Assess this cell for malaria.
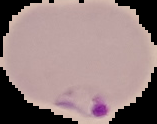
It is parasitized.

From a thin blood film. Cell region segmented out of the field of view; the surrounding area is masked to black. Image is 157×124 pixels.